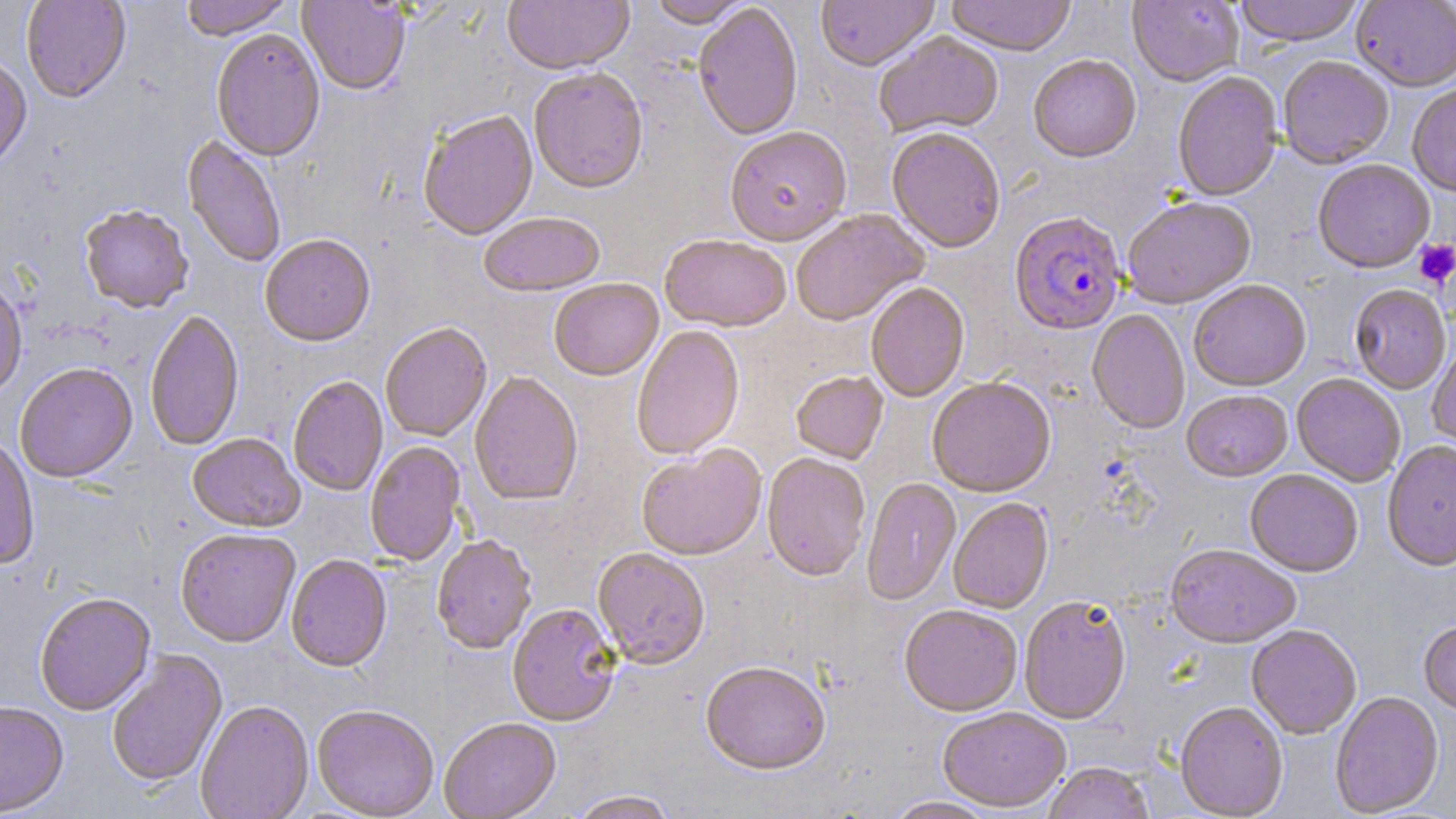

slide_level_diagnosis: Plasmodium falciparum
uninfected_red_blood_cell_locations: 'approximate bounding boxes as named x1/y1/x2/y2 corners in pixels: (x1=21, y1=0, x2=131, y2=104), (x1=180, y1=0, x2=295, y2=42), (x1=502, y1=0, x2=634, y2=77), (x1=816, y1=0, x2=939, y2=74), (x1=945, y1=0, x2=1076, y2=58), (x1=1128, y1=0, x2=1243, y2=88), (x1=1234, y1=0, x2=1364, y2=49), (x1=297, y1=1, x2=410, y2=98), (x1=647, y1=1, x2=752, y2=30), (x1=1351, y1=1, x2=1456, y2=93), (x1=693, y1=4, x2=803, y2=143), (x1=211, y1=31, x2=325, y2=164), (x1=874, y1=32, x2=1004, y2=141), (x1=1028, y1=56, x2=1141, y2=165), (x1=1278, y1=57, x2=1394, y2=170), (x1=0, y1=58, x2=32, y2=173), (x1=529, y1=70, x2=648, y2=197), (x1=1173, y1=72, x2=1283, y2=203), (x1=1407, y1=84, x2=1456, y2=198), (x1=419, y1=113, x2=539, y2=243), (x1=725, y1=129, x2=853, y2=249), (x1=886, y1=130, x2=1005, y2=255), (x1=181, y1=136, x2=286, y2=269), (x1=1313, y1=161, x2=1434, y2=275), (x1=1123, y1=198, x2=1256, y2=310), (x1=80, y1=207, x2=194, y2=316), (x1=790, y1=210, x2=928, y2=328), (x1=479, y1=215, x2=606, y2=299), (x1=260, y1=237, x2=375, y2=350), (x1=660, y1=237, x2=790, y2=334), (x1=0, y1=280, x2=28, y2=401), (x1=549, y1=280, x2=664, y2=383), (x1=1189, y1=281, x2=1311, y2=393), (x1=866, y1=285, x2=969, y2=404), (x1=1349, y1=286, x2=1451, y2=395), (x1=1087, y1=310, x2=1190, y2=435), (x1=145, y1=312, x2=245, y2=452), (x1=380, y1=325, x2=492, y2=443), (x1=632, y1=327, x2=745, y2=461), (x1=1427, y1=342, x2=1456, y2=452), (x1=15, y1=364, x2=137, y2=486), (x1=791, y1=373, x2=889, y2=466), (x1=469, y1=374, x2=583, y2=508), (x1=1291, y1=374, x2=1405, y2=488), (x1=288, y1=378, x2=388, y2=497), (x1=928, y1=380, x2=1056, y2=499), (x1=1181, y1=392, x2=1293, y2=483), (x1=187, y1=436, x2=305, y2=534), (x1=0, y1=437, x2=39, y2=572), (x1=365, y1=441, x2=466, y2=568), (x1=1383, y1=442, x2=1456, y2=573), (x1=636, y1=447, x2=767, y2=562), (x1=762, y1=455, x2=871, y2=584), (x1=1245, y1=470, x2=1362, y2=578), (x1=861, y1=479, x2=961, y2=607), (x1=948, y1=499, x2=1054, y2=614), (x1=175, y1=530, x2=301, y2=649), (x1=432, y1=537, x2=537, y2=656), (x1=1164, y1=546, x2=1301, y2=650), (x1=592, y1=550, x2=710, y2=671), (x1=286, y1=556, x2=392, y2=674), (x1=35, y1=595, x2=156, y2=716), (x1=1020, y1=598, x2=1132, y2=726), (x1=507, y1=605, x2=621, y2=727), (x1=900, y1=607, x2=1022, y2=718), (x1=1418, y1=621, x2=1456, y2=718), (x1=1246, y1=625, x2=1362, y2=740), (x1=107, y1=651, x2=228, y2=789), (x1=700, y1=664, x2=830, y2=777), (x1=1330, y1=692, x2=1444, y2=817), (x1=0, y1=702, x2=69, y2=818), (x1=195, y1=703, x2=314, y2=819), (x1=1175, y1=703, x2=1288, y2=817), (x1=312, y1=706, x2=439, y2=819), (x1=938, y1=708, x2=1070, y2=813), (x1=439, y1=720, x2=561, y2=819), (x1=1043, y1=764, x2=1156, y2=819), (x1=567, y1=791, x2=678, y2=819), (x1=883, y1=797, x2=997, y2=819)'
field_of_view: one of a larger specimen
magnification: 1000x
stain: May-Grünwald-Giemsa
preparation: thin blood smear
platelet_locations: 'approximate bounding boxes as named x1/y1/x2/y2 corners in pixels: (x1=1414, y1=239, x2=1456, y2=287)'
image_size: 1456×819 pixels
plasmodium_falciparum_infected_red_blood_cell_locations: 'approximate bounding boxes as named x1/y1/x2/y2 corners in pixels: (x1=1009, y1=213, x2=1126, y2=337)'
modality: light microscopy